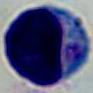

Summary:
  - Identification: leukocyte
  - Modality: micrograph
  - Magnification: 1000x